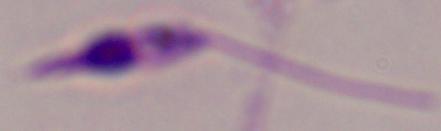

Summary:
  - Modality: photomicrograph
  - Magnification: 1000x
  - Identification: Leishmania